Outline each blood parasite and name the species.
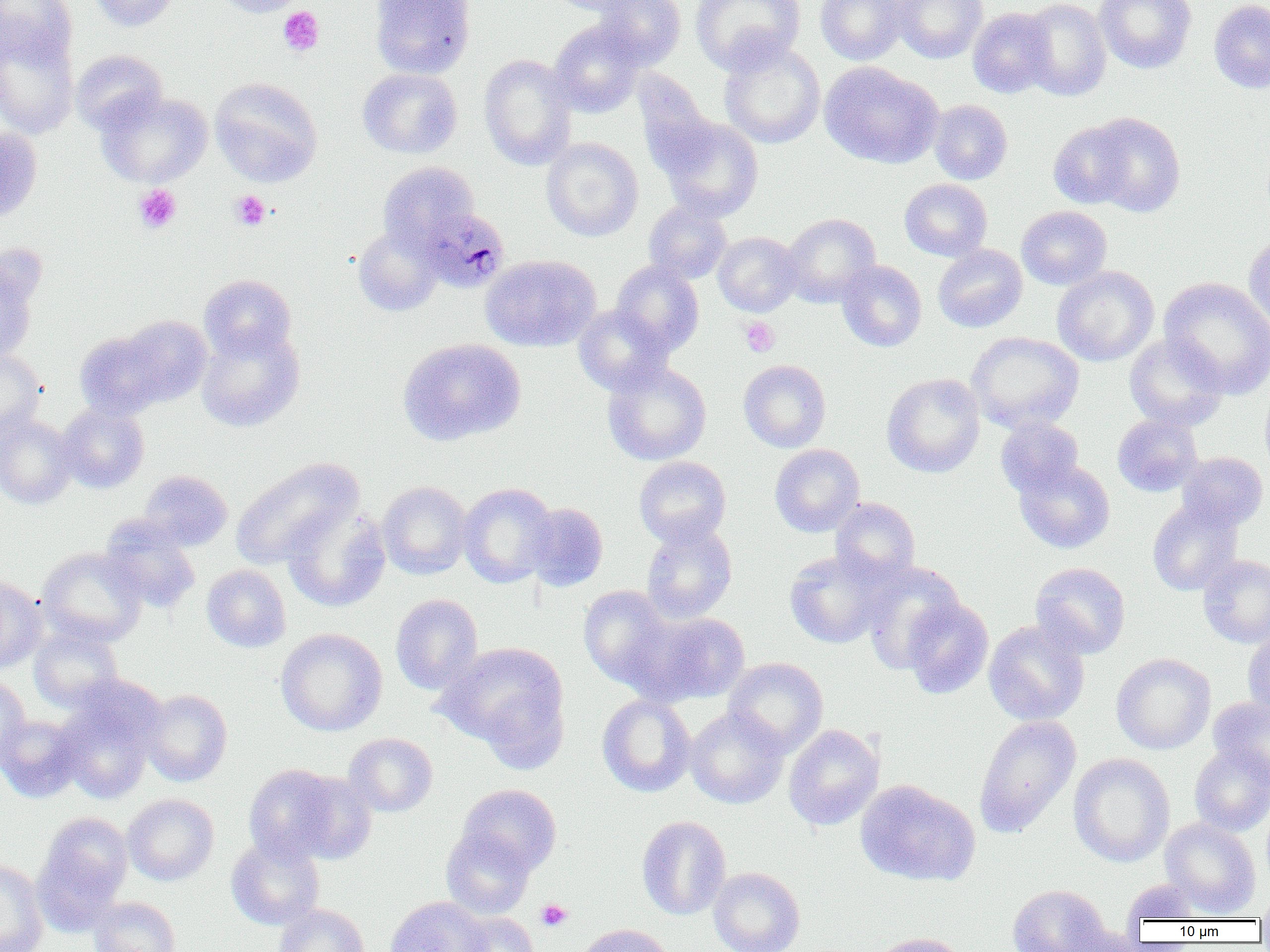
Approximate bounding boxes as named x1/y1/x2/y2 corners in pixels.
Plasmodium malariae-infected red blood cells: (x1=421, y1=215, x2=511, y2=299).
No Plasmodium falciparum, Plasmodium ovale, Plasmodium vivax, Babesia divergens, or Trypanosoma brucei observed.

Summary:
  - Platelet locations: (x1=278, y1=7, x2=324, y2=56), (x1=133, y1=184, x2=182, y2=234), (x1=230, y1=190, x2=271, y2=230), (x1=739, y1=316, x2=780, y2=357), (x1=536, y1=899, x2=572, y2=931)
  - Uninfected red blood cell locations: (x1=0, y1=0, x2=78, y2=67), (x1=89, y1=0, x2=180, y2=31), (x1=211, y1=0, x2=308, y2=17), (x1=370, y1=0, x2=476, y2=78), (x1=548, y1=0, x2=644, y2=16), (x1=592, y1=0, x2=686, y2=68), (x1=691, y1=0, x2=805, y2=74), (x1=815, y1=0, x2=910, y2=65), (x1=892, y1=0, x2=988, y2=63), (x1=1020, y1=0, x2=1111, y2=101), (x1=1094, y1=0, x2=1197, y2=74), (x1=1209, y1=1, x2=1270, y2=93), (x1=967, y1=7, x2=1056, y2=98), (x1=548, y1=20, x2=646, y2=117), (x1=0, y1=28, x2=79, y2=138), (x1=719, y1=40, x2=825, y2=149), (x1=71, y1=49, x2=167, y2=134), (x1=478, y1=53, x2=577, y2=170), (x1=819, y1=61, x2=943, y2=169), (x1=357, y1=68, x2=462, y2=158), (x1=210, y1=77, x2=323, y2=187), (x1=97, y1=92, x2=213, y2=187), (x1=929, y1=100, x2=1013, y2=184), (x1=1084, y1=112, x2=1186, y2=217), (x1=655, y1=115, x2=764, y2=222), (x1=1049, y1=123, x2=1135, y2=208), (x1=0, y1=126, x2=43, y2=221), (x1=541, y1=137, x2=643, y2=242), (x1=378, y1=162, x2=479, y2=252), (x1=900, y1=179, x2=992, y2=261), (x1=644, y1=201, x2=732, y2=283), (x1=1016, y1=206, x2=1111, y2=290), (x1=781, y1=213, x2=881, y2=307), (x1=352, y1=226, x2=443, y2=316), (x1=713, y1=232, x2=802, y2=316), (x1=1244, y1=232, x2=1270, y2=334), (x1=933, y1=244, x2=1027, y2=332), (x1=481, y1=255, x2=600, y2=351), (x1=0, y1=259, x2=39, y2=363), (x1=836, y1=260, x2=927, y2=352), (x1=611, y1=261, x2=704, y2=356), (x1=1052, y1=266, x2=1158, y2=366), (x1=199, y1=274, x2=297, y2=361), (x1=1159, y1=276, x2=1270, y2=398), (x1=573, y1=304, x2=673, y2=396), (x1=118, y1=315, x2=212, y2=406), (x1=196, y1=325, x2=304, y2=432), (x1=74, y1=329, x2=172, y2=420), (x1=966, y1=332, x2=1084, y2=433), (x1=1124, y1=333, x2=1228, y2=431), (x1=397, y1=338, x2=526, y2=446), (x1=0, y1=349, x2=46, y2=440), (x1=738, y1=359, x2=831, y2=452), (x1=602, y1=360, x2=712, y2=466), (x1=882, y1=373, x2=985, y2=478), (x1=1260, y1=381, x2=1270, y2=479), (x1=57, y1=404, x2=149, y2=493), (x1=0, y1=411, x2=77, y2=509), (x1=1112, y1=415, x2=1203, y2=497), (x1=995, y1=418, x2=1084, y2=497), (x1=770, y1=444, x2=865, y2=537), (x1=1177, y1=452, x2=1268, y2=531), (x1=231, y1=456, x2=363, y2=570), (x1=634, y1=456, x2=731, y2=548), (x1=1014, y1=458, x2=1115, y2=553), (x1=139, y1=470, x2=232, y2=551), (x1=377, y1=481, x2=472, y2=579), (x1=457, y1=483, x2=557, y2=587), (x1=830, y1=497, x2=920, y2=584), (x1=1147, y1=500, x2=1243, y2=596), (x1=524, y1=502, x2=608, y2=592), (x1=282, y1=505, x2=391, y2=612), (x1=100, y1=517, x2=200, y2=614), (x1=640, y1=520, x2=738, y2=623), (x1=37, y1=547, x2=147, y2=647), (x1=784, y1=549, x2=891, y2=649), (x1=1198, y1=555, x2=1270, y2=647), (x1=861, y1=562, x2=965, y2=671), (x1=1030, y1=562, x2=1131, y2=658), (x1=202, y1=565, x2=291, y2=652), (x1=0, y1=576, x2=46, y2=673), (x1=578, y1=585, x2=675, y2=690), (x1=390, y1=594, x2=483, y2=694), (x1=900, y1=597, x2=993, y2=699), (x1=634, y1=611, x2=752, y2=705), (x1=984, y1=619, x2=1090, y2=726), (x1=29, y1=626, x2=124, y2=713), (x1=276, y1=628, x2=387, y2=736), (x1=1243, y1=629, x2=1270, y2=719), (x1=437, y1=641, x2=569, y2=755), (x1=1111, y1=653, x2=1215, y2=754), (x1=724, y1=658, x2=828, y2=757), (x1=0, y1=674, x2=31, y2=766), (x1=55, y1=689, x2=161, y2=805), (x1=140, y1=689, x2=232, y2=786), (x1=597, y1=694, x2=696, y2=797), (x1=1208, y1=697, x2=1270, y2=784), (x1=685, y1=707, x2=789, y2=809), (x1=0, y1=714, x2=85, y2=803), (x1=973, y1=715, x2=1081, y2=837), (x1=783, y1=724, x2=884, y2=830), (x1=343, y1=732, x2=438, y2=817), (x1=1189, y1=743, x2=1270, y2=836), (x1=1068, y1=753, x2=1174, y2=867), (x1=244, y1=764, x2=342, y2=863), (x1=287, y1=771, x2=377, y2=864), (x1=855, y1=779, x2=980, y2=887), (x1=457, y1=784, x2=561, y2=875), (x1=122, y1=794, x2=219, y2=886), (x1=33, y1=810, x2=133, y2=922), (x1=636, y1=816, x2=731, y2=920), (x1=1160, y1=818, x2=1261, y2=916), (x1=440, y1=827, x2=536, y2=920), (x1=226, y1=835, x2=325, y2=930), (x1=0, y1=859, x2=49, y2=952), (x1=708, y1=866, x2=805, y2=952), (x1=1120, y1=879, x2=1213, y2=924), (x1=1006, y1=884, x2=1114, y2=951), (x1=1255, y1=888, x2=1270, y2=926), (x1=88, y1=896, x2=180, y2=952), (x1=386, y1=896, x2=493, y2=952), (x1=273, y1=903, x2=370, y2=952), (x1=455, y1=912, x2=539, y2=952), (x1=573, y1=924, x2=673, y2=952), (x1=866, y1=932, x2=970, y2=952)
  - Slide-level diagnosis: Plasmodium malariae
  - Modality: optical microscopy
  - Image size: 1270×952 pixels
  - Preparation: thin blood smear
  - Magnification: 1000x
  - Field of view: single